Outline each blood parasite and name the species.
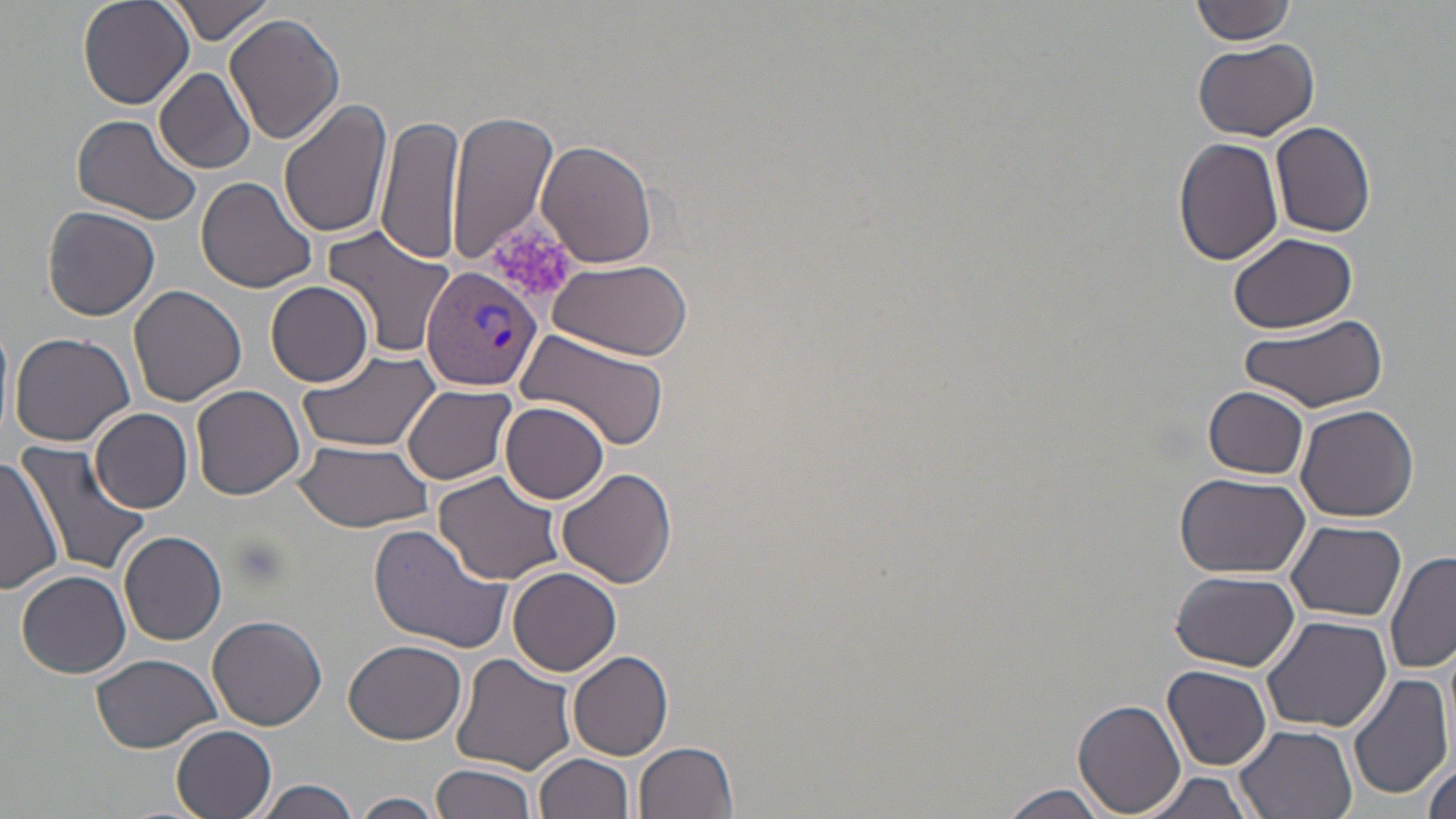
Approximate bounding boxes as (x1, y1, x2, y2) in pixels.
Plasmodium vivax-infected red blood cells: (421, 266, 541, 391).
No Plasmodium falciparum, Plasmodium ovale, Plasmodium malariae, Babesia divergens, or Trypanosoma brucei observed.

Platelet locations: (490, 224, 580, 304). Uninfected red blood cell locations: (78, 0, 195, 110), (169, 0, 276, 45), (1190, 1, 1296, 45), (225, 14, 346, 146), (1192, 37, 1316, 141), (155, 67, 256, 174), (278, 97, 393, 239), (446, 109, 560, 266), (72, 113, 202, 224), (378, 113, 464, 266), (58, 114, 184, 321), (1271, 120, 1377, 239), (1174, 136, 1284, 266), (536, 140, 656, 268), (194, 177, 319, 294), (42, 205, 161, 321), (324, 224, 459, 357), (1230, 232, 1357, 334), (545, 259, 694, 362), (265, 279, 374, 386), (128, 286, 246, 407), (1236, 314, 1388, 414), (0, 317, 14, 441), (9, 330, 135, 447), (515, 330, 669, 454), (296, 346, 442, 454), (192, 383, 305, 499), (403, 383, 516, 485), (1204, 386, 1310, 479), (501, 401, 611, 503), (1294, 401, 1420, 522), (90, 407, 193, 512), (16, 441, 148, 577), (294, 442, 436, 532), (0, 455, 62, 596), (556, 467, 678, 590), (432, 468, 568, 586), (1176, 472, 1312, 580), (1287, 520, 1405, 621), (366, 523, 513, 652), (119, 528, 228, 645), (1385, 552, 1456, 676), (16, 568, 131, 678), (509, 568, 622, 676), (1170, 570, 1298, 673), (208, 613, 327, 731), (1259, 614, 1390, 733), (344, 640, 465, 745), (568, 650, 674, 762), (451, 652, 580, 775), (90, 654, 222, 753), (1163, 665, 1272, 769), (1348, 671, 1453, 801), (1074, 699, 1186, 814), (170, 722, 279, 819), (1235, 724, 1358, 819), (635, 741, 740, 819), (1420, 745, 1456, 819), (534, 752, 636, 819), (432, 763, 539, 819), (1135, 769, 1257, 819), (258, 779, 361, 819), (996, 786, 1113, 819), (352, 792, 445, 819). Slide-level diagnosis: Plasmodium vivax. May-Grünwald-Giemsa stain. Light microscopy. Image is 1456×819 pixels. One field of a larger specimen. Thin blood film. Captured at 1000x magnification.